Assess this cell for malaria.
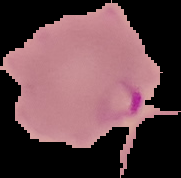
Parasitized.

The area outside the segmented cell region is set to black. Image is 181×178 pixels. From a thin blood film.